Point out each Plasmodium parasite.
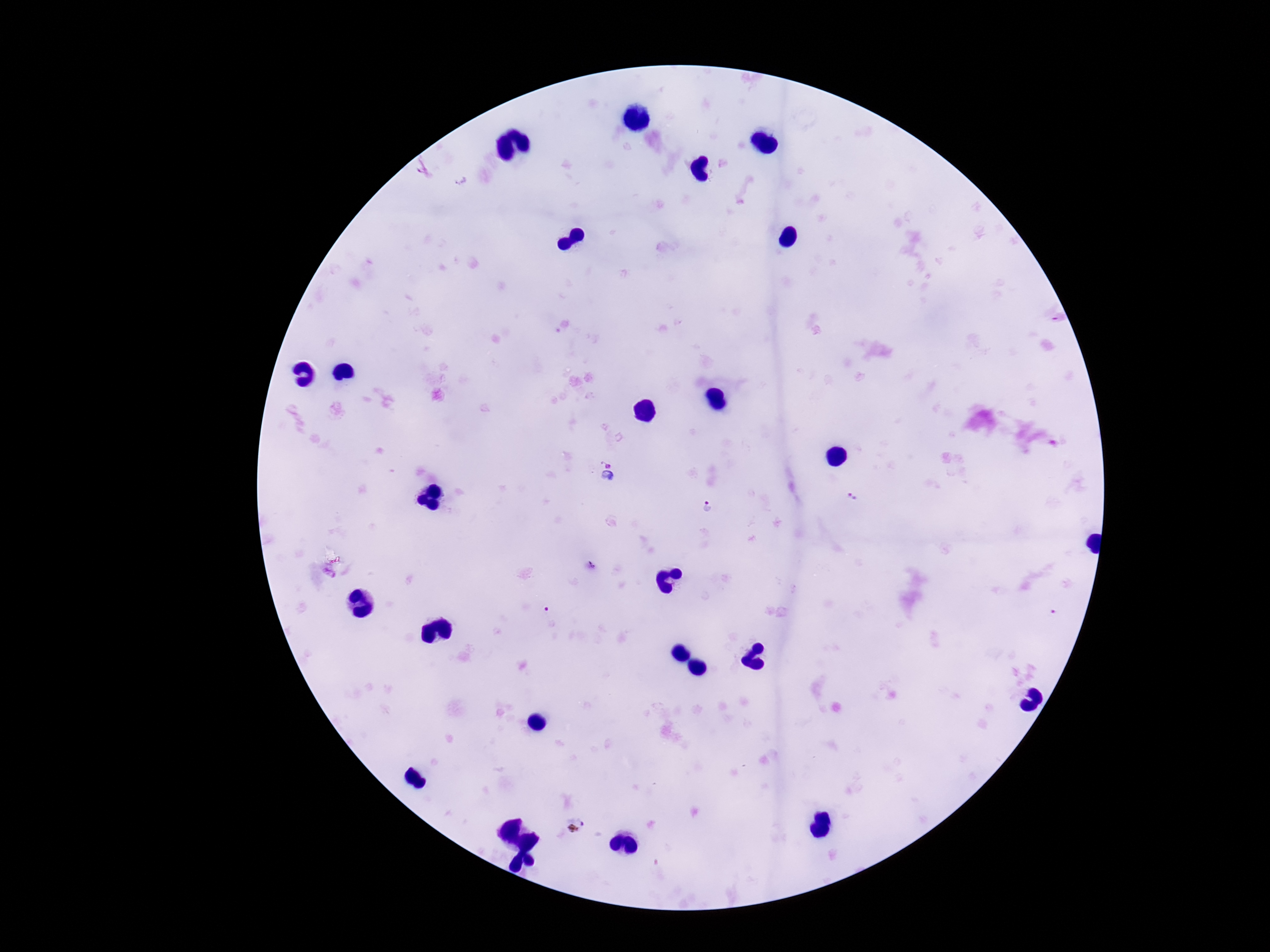

Approximate centers as [x, y] in pixels.
Plasmodium parasites: [609, 474], [853, 495], [708, 506], [589, 567].

capture = smartphone camera through the microscope eyepiece
field of view = one from this slide
stain = Giemsa
patient malaria status = positive
image size = 1270×952 pixels
magnification = 100x
preparation = thick peripheral-blood smear